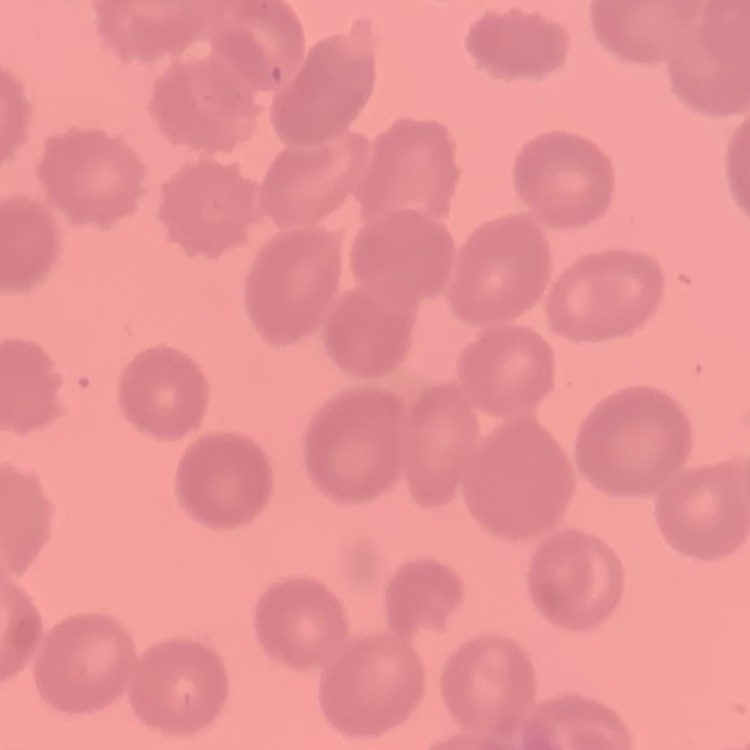
red blood cell morphology = no rouleaux formation
stain = Field's or Giemsa
image type = one tile cut from a larger photomicrograph
preparation = thin peripheral smear